Give the position of every Plasmodium parasite visible.
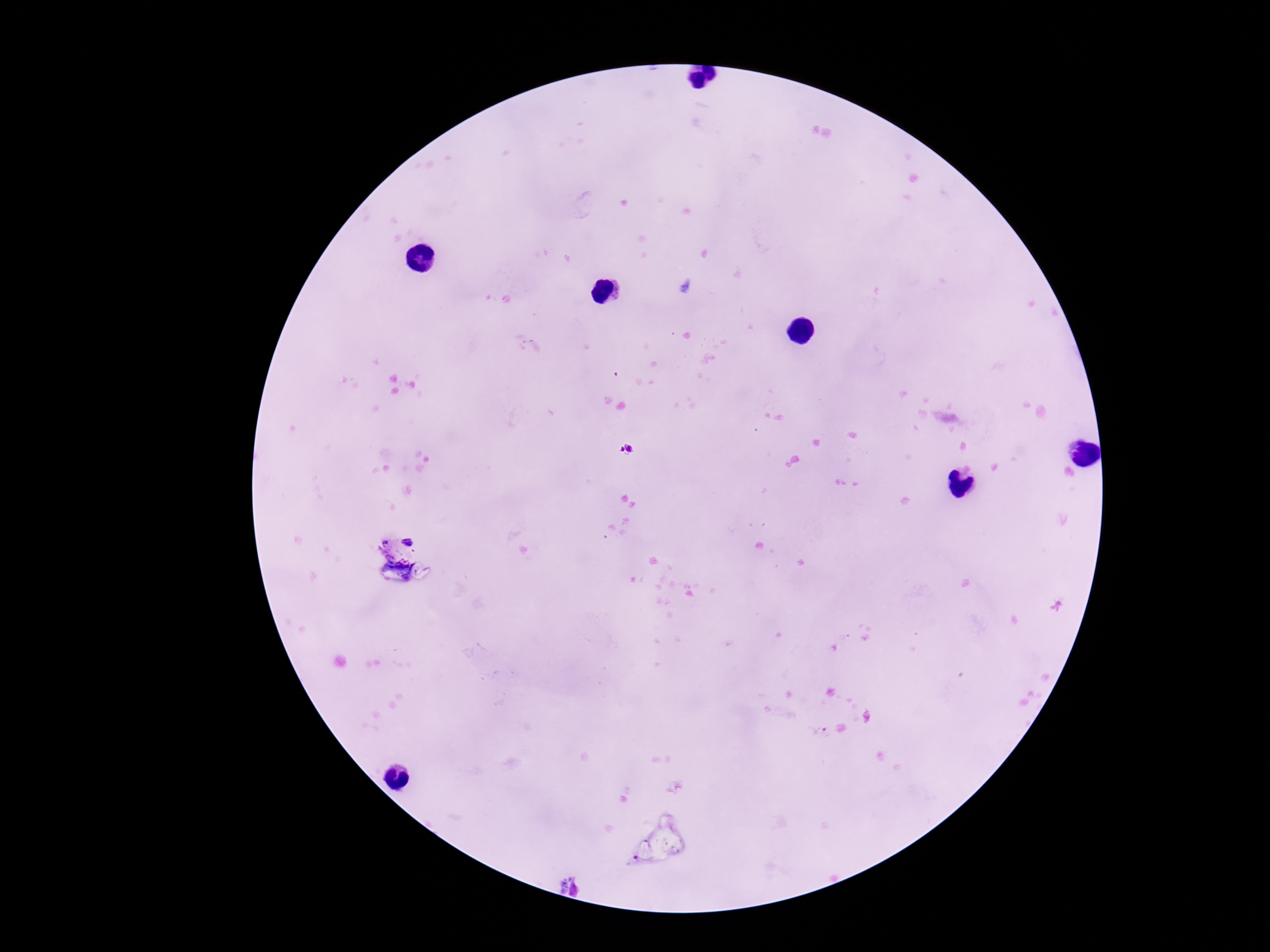
Approximate object centers, in pixels from the top-left corner.
Plasmodium parasites: (x=627, y=450), (x=408, y=541).

Summary:
  - Patient malaria status: infected
  - Preparation: thick peripheral-blood smear
  - Stain: Giemsa
  - Magnification: 100x
  - Capture: smartphone camera through the microscope eyepiece
  - Field of view: one from this slide
  - Image size: 1270×952 pixels